State the blood parasite species.
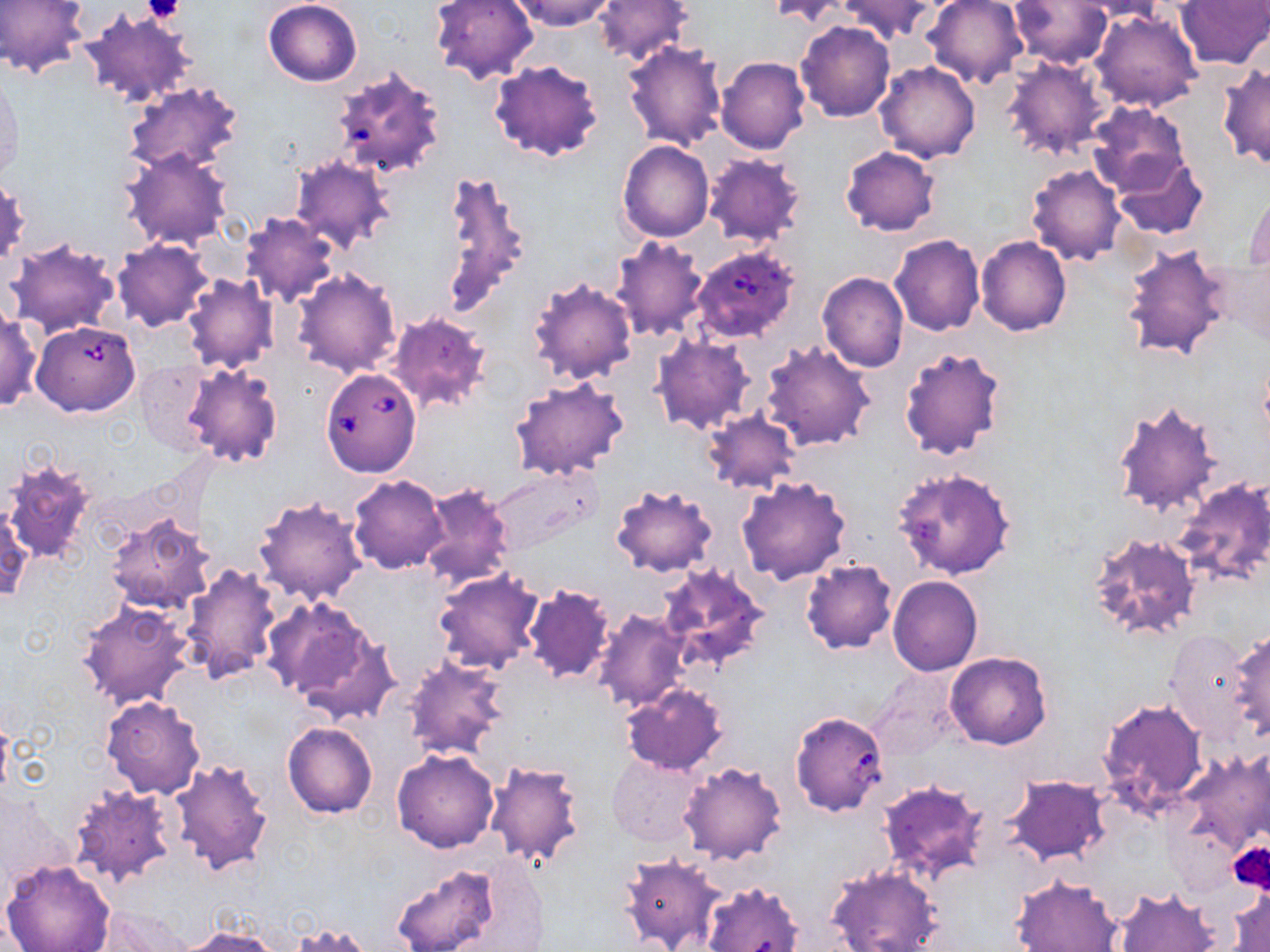
Babesia divergens.

Summary:
  - Coordinate format: approximate bounding boxes as named x1/y1/x2/y2 corners in pixels
  - Platelet locations: (x1=143, y1=0, x2=186, y2=25), (x1=1230, y1=842, x2=1270, y2=892)
  - Uninfected red blood cell locations: (x1=0, y1=0, x2=90, y2=79), (x1=263, y1=0, x2=363, y2=86), (x1=430, y1=0, x2=538, y2=85), (x1=508, y1=0, x2=619, y2=30), (x1=594, y1=0, x2=693, y2=66), (x1=766, y1=0, x2=853, y2=26), (x1=921, y1=0, x2=1028, y2=88), (x1=1010, y1=0, x2=1113, y2=68), (x1=1071, y1=0, x2=1168, y2=21), (x1=1175, y1=0, x2=1269, y2=70), (x1=837, y1=1, x2=938, y2=43), (x1=1090, y1=7, x2=1203, y2=112), (x1=80, y1=8, x2=199, y2=109), (x1=795, y1=21, x2=895, y2=121), (x1=623, y1=39, x2=728, y2=151), (x1=1001, y1=55, x2=1111, y2=162), (x1=717, y1=57, x2=811, y2=154), (x1=488, y1=59, x2=604, y2=162), (x1=875, y1=61, x2=981, y2=163), (x1=1217, y1=65, x2=1270, y2=170), (x1=331, y1=71, x2=441, y2=177), (x1=0, y1=73, x2=22, y2=184), (x1=124, y1=82, x2=243, y2=175), (x1=1087, y1=102, x2=1190, y2=196), (x1=617, y1=140, x2=715, y2=242), (x1=841, y1=145, x2=941, y2=236), (x1=123, y1=147, x2=234, y2=250), (x1=702, y1=152, x2=807, y2=247), (x1=289, y1=154, x2=395, y2=253), (x1=1111, y1=154, x2=1207, y2=240), (x1=1026, y1=163, x2=1125, y2=266), (x1=438, y1=170, x2=531, y2=318), (x1=0, y1=176, x2=29, y2=268), (x1=1244, y1=188, x2=1270, y2=274), (x1=241, y1=212, x2=341, y2=307), (x1=889, y1=234, x2=984, y2=336), (x1=610, y1=235, x2=709, y2=343), (x1=975, y1=237, x2=1071, y2=336), (x1=5, y1=239, x2=121, y2=337), (x1=113, y1=240, x2=212, y2=331), (x1=1119, y1=241, x2=1233, y2=364), (x1=1225, y1=259, x2=1269, y2=346), (x1=293, y1=269, x2=401, y2=378), (x1=817, y1=273, x2=909, y2=372), (x1=182, y1=274, x2=279, y2=374), (x1=527, y1=274, x2=637, y2=386), (x1=0, y1=309, x2=41, y2=412), (x1=386, y1=310, x2=493, y2=414), (x1=650, y1=334, x2=756, y2=435), (x1=759, y1=340, x2=876, y2=452), (x1=898, y1=346, x2=1007, y2=461), (x1=132, y1=361, x2=217, y2=456), (x1=181, y1=363, x2=283, y2=467), (x1=510, y1=376, x2=629, y2=480), (x1=1112, y1=401, x2=1223, y2=517), (x1=702, y1=409, x2=802, y2=497), (x1=3, y1=456, x2=96, y2=564), (x1=891, y1=465, x2=1016, y2=581), (x1=486, y1=467, x2=601, y2=556), (x1=348, y1=475, x2=448, y2=574), (x1=737, y1=477, x2=851, y2=585), (x1=1172, y1=477, x2=1270, y2=588), (x1=609, y1=482, x2=717, y2=578), (x1=418, y1=484, x2=517, y2=592), (x1=254, y1=495, x2=367, y2=605), (x1=1, y1=501, x2=31, y2=606), (x1=104, y1=514, x2=216, y2=616), (x1=1086, y1=530, x2=1202, y2=643), (x1=801, y1=560, x2=897, y2=654), (x1=178, y1=563, x2=283, y2=686), (x1=654, y1=563, x2=772, y2=673), (x1=432, y1=570, x2=544, y2=675), (x1=887, y1=576, x2=983, y2=676), (x1=521, y1=583, x2=614, y2=684), (x1=76, y1=600, x2=196, y2=709), (x1=268, y1=600, x2=390, y2=714), (x1=593, y1=607, x2=692, y2=714), (x1=1227, y1=626, x2=1270, y2=745), (x1=1162, y1=627, x2=1253, y2=747), (x1=946, y1=652, x2=1052, y2=749), (x1=402, y1=654, x2=509, y2=762), (x1=868, y1=670, x2=961, y2=762), (x1=621, y1=682, x2=729, y2=774), (x1=100, y1=696, x2=206, y2=799), (x1=1097, y1=698, x2=1208, y2=812), (x1=282, y1=722, x2=377, y2=818), (x1=1173, y1=748, x2=1268, y2=866), (x1=391, y1=749, x2=500, y2=853), (x1=607, y1=753, x2=705, y2=846), (x1=169, y1=757, x2=273, y2=878), (x1=482, y1=759, x2=586, y2=869), (x1=678, y1=761, x2=788, y2=865), (x1=1003, y1=775, x2=1109, y2=865), (x1=877, y1=778, x2=989, y2=881), (x1=69, y1=782, x2=179, y2=888), (x1=1231, y1=839, x2=1270, y2=900), (x1=619, y1=852, x2=726, y2=952), (x1=1, y1=858, x2=116, y2=952), (x1=388, y1=860, x2=521, y2=952), (x1=825, y1=865, x2=944, y2=952), (x1=1010, y1=875, x2=1125, y2=952), (x1=701, y1=880, x2=804, y2=952), (x1=1229, y1=882, x2=1269, y2=952), (x1=1114, y1=887, x2=1220, y2=952), (x1=290, y1=923, x2=373, y2=951), (x1=176, y1=927, x2=286, y2=952)
  - Babesia divergens-infected red blood cell locations: (x1=690, y1=245, x2=801, y2=344), (x1=32, y1=319, x2=140, y2=416), (x1=320, y1=368, x2=422, y2=478)
  - Image size: 1270×952 pixels
  - Preparation: thin blood smear
  - Field of view: one of a larger specimen
  - Magnification: 1000x
  - Modality: light microscopy
  - Stain: May-Grünwald-Giemsa